Assess the morphology of the red blood cells.
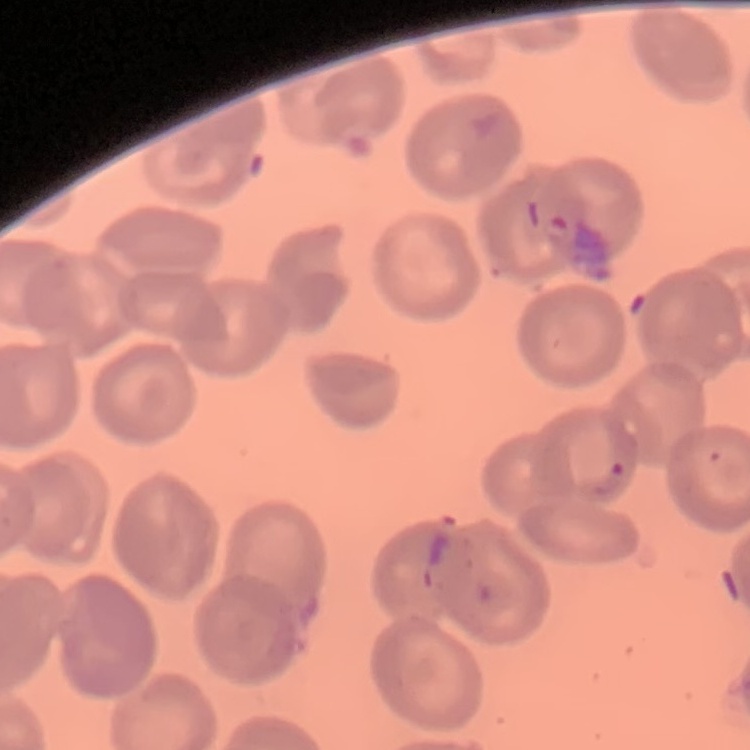
They show no rouleaux formation.

Summary:
  - Image type: square crop of a larger photomicrograph
  - Preparation: thin blood smear
  - Stain: Field's or Giemsa